Name the parasite shown.
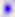
This is Toxoplasma gondii.

modality: micrograph
magnification: 400x